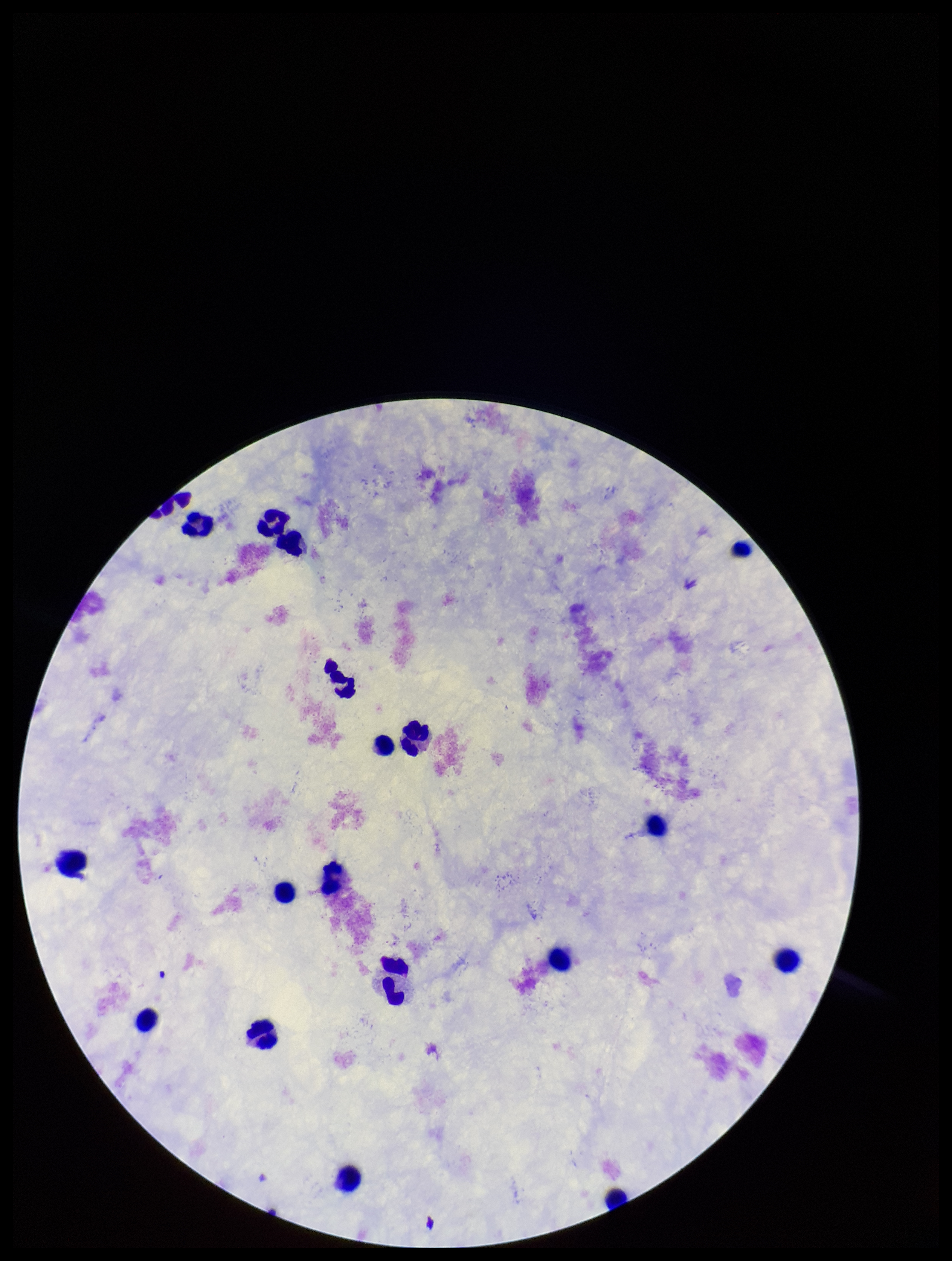

Summary:
  - Patient malaria status: negative
  - Field of view: single
  - Stain: Giemsa
  - Plasmodium parasites: none identified
  - Parasite count: 0
  - Preparation: thick smear
  - Leukocyte count: 19
  - Capture: smartphone photograph through the microscope eyepiece
  - Image size: 952×1261 pixels